Assess the morphology of the red blood cells.
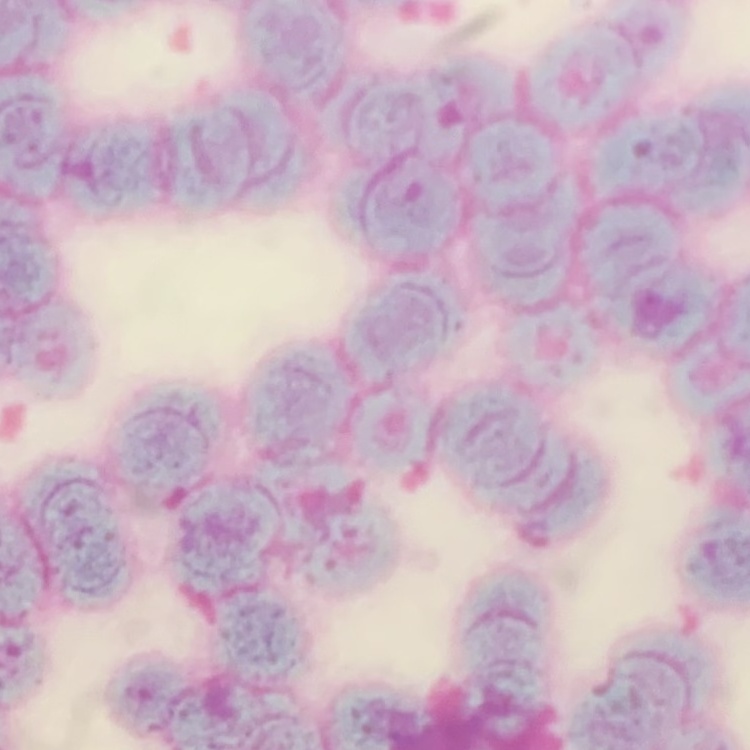

They show rouleaux formation.

image_type: one tile cut from a larger photomicrograph
stain: Field's or Giemsa
preparation: thin peripheral smear